Classify this cell by malaria status.
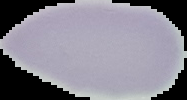

It is uninfected.

The area outside the segmented cell region is set to black. From a thin blood smear. Image is 187×100 pixels.